Identify the preparation type.
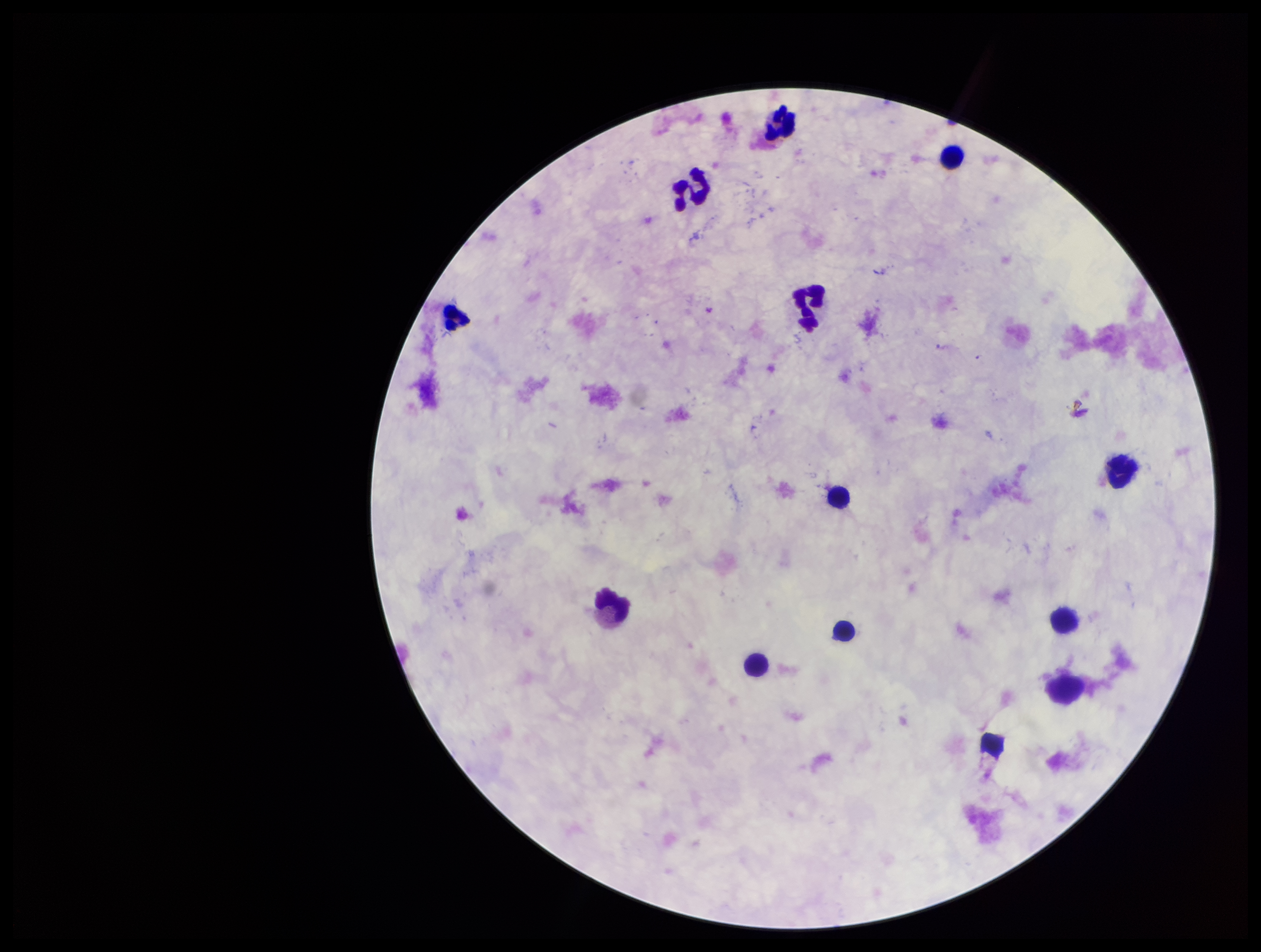

A thick smear.

Stained with Giemsa. Patient malaria status: negative. Plasmodium parasites: none identified. One field from this slide. Parasite count: 0. Image is 1261×952 pixels. Leukocyte count: 12. Photographed through the microscope eyepiece with a smartphone camera.